Assess this cell for malaria.
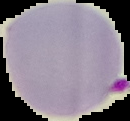

Parasitized.

From a thin blood film. The area outside the segmented cell region is set to black. Image is 130×121 pixels.